Classify this cell by malaria status.
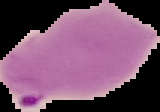
Parasitized.

preparation = thin blood film
image type = segmented cell region on a black background
image size = 160×112 pixels